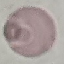
Result: no malaria parasites seen. Thin smear of blood. Photographed with a smartphone camera at the microscope eyepiece. Cell patch, automatically extracted from a larger field of view and resized to 64 × 64 pixels. Giemsa stain.